Assess the morphology of the erythrocytes.
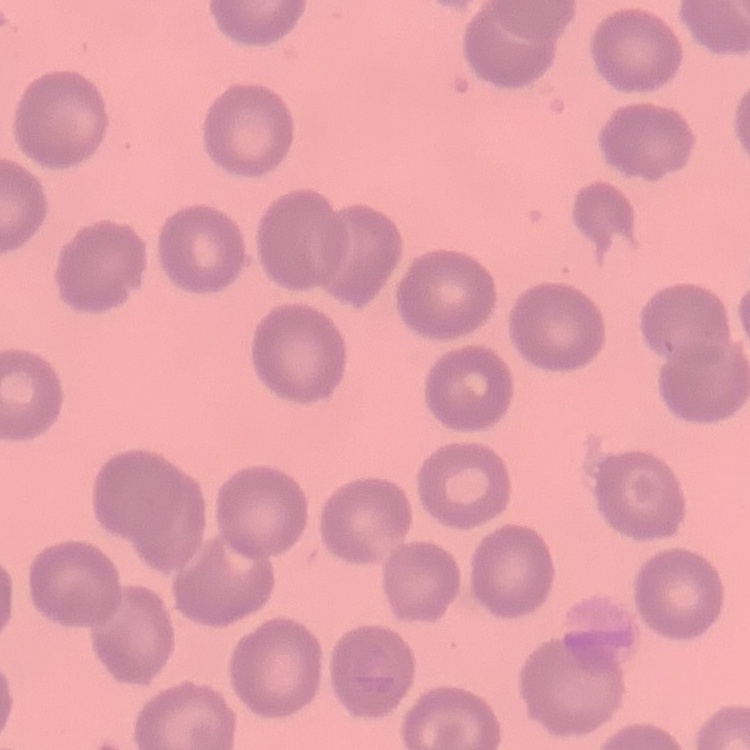
They show no rouleaux formation.

Square crop of a larger photomicrograph. Stained with either Field's or Giemsa. Thin peripheral smear.